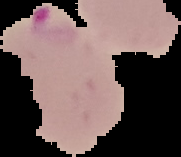
The area outside the segmented cell region is set to black. From a thin blood smear. Image is 181×157 pixels. Result: malaria parasites identified.